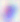
Summary:
  - Modality: micrograph
  - Identification: Toxoplasma gondii
  - Magnification: 400x